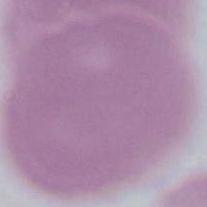 An erythrocyte is shown. 1000x magnification. Photomicrograph.